Identify the parasite.
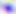
This is Toxoplasma gondii.

{
  "magnification": "400x",
  "modality": "photomicrograph"
}